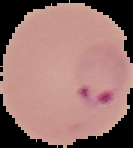

Result: malaria parasites detected. Image is 133×148 pixels. Segmented cell region on a black background. From a thin blood film.